Outline each Trypanosoma brucei.
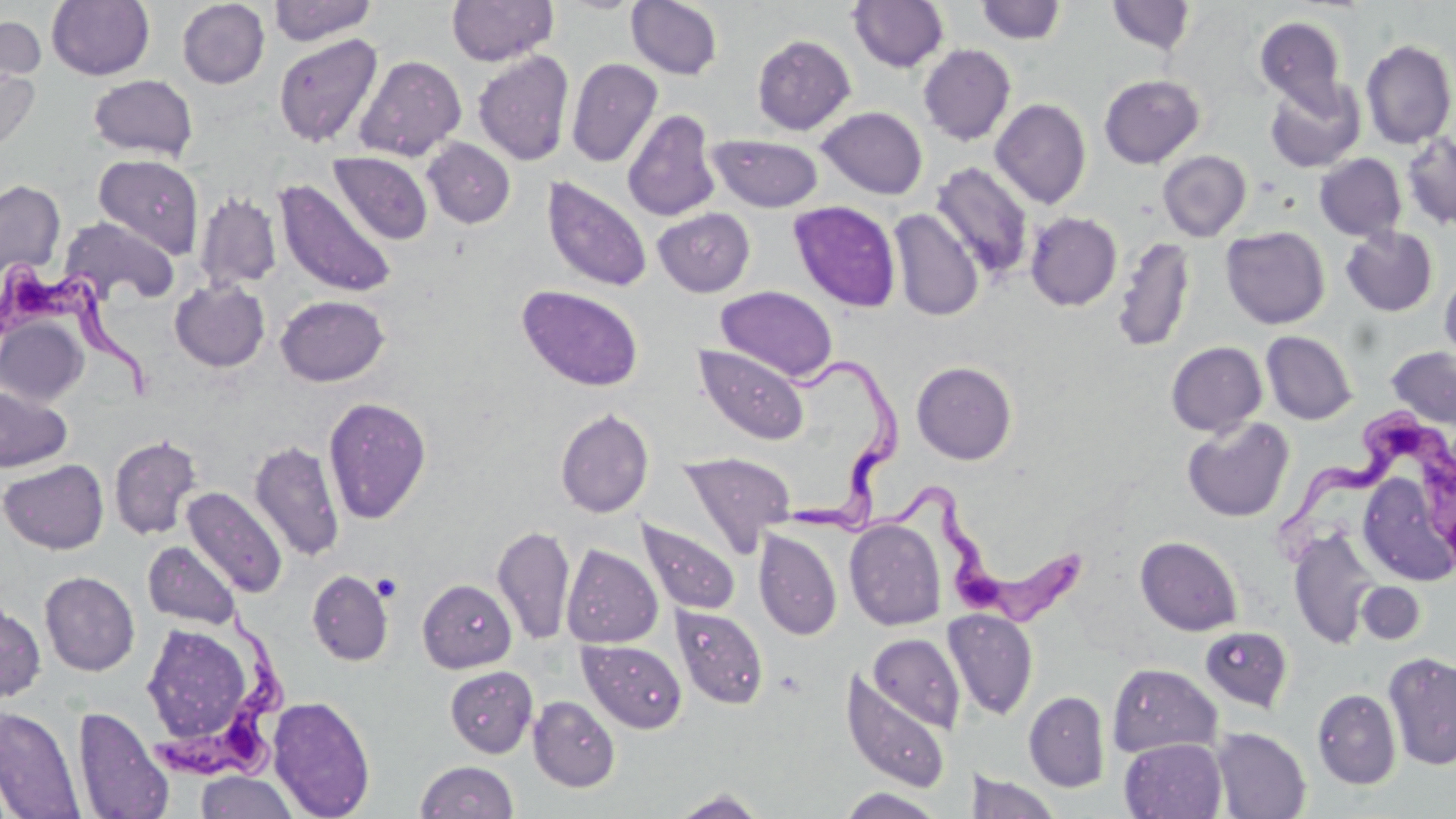
Approximate bounding boxes as named x1/y1/x2/y2 corners in pixels.
Trypanosoma brucei: (x1=1, y1=257, x2=162, y2=401), (x1=771, y1=350, x2=910, y2=549), (x1=1279, y1=411, x2=1453, y2=558), (x1=878, y1=484, x2=1083, y2=635), (x1=151, y1=608, x2=290, y2=785).

{
  "slide_level_diagnosis": "Trypanosoma brucei",
  "field_of_view": "one of a larger specimen",
  "modality": "light microscopy",
  "image_size": "1456×819 pixels",
  "magnification": "1000x",
  "uninfected_red_blood_cell_locations": "approximate bounding boxes as named x1/y1/x2/y2 corners in pixels: (x1=47, y1=0, x2=154, y2=80), (x1=269, y1=0, x2=377, y2=45), (x1=447, y1=0, x2=559, y2=66), (x1=627, y1=0, x2=723, y2=79), (x1=848, y1=0, x2=949, y2=73), (x1=177, y1=1, x2=269, y2=88), (x1=976, y1=1, x2=1067, y2=44), (x1=1106, y1=1, x2=1197, y2=55), (x1=0, y1=14, x2=46, y2=94), (x1=1255, y1=16, x2=1348, y2=115), (x1=273, y1=33, x2=383, y2=147), (x1=751, y1=34, x2=856, y2=134), (x1=1361, y1=39, x2=1455, y2=149), (x1=918, y1=44, x2=1016, y2=145), (x1=472, y1=49, x2=574, y2=166), (x1=354, y1=55, x2=467, y2=162), (x1=566, y1=57, x2=662, y2=168), (x1=0, y1=61, x2=40, y2=159), (x1=88, y1=74, x2=198, y2=160), (x1=1098, y1=74, x2=1205, y2=168), (x1=1264, y1=77, x2=1363, y2=172), (x1=991, y1=98, x2=1091, y2=209), (x1=817, y1=106, x2=928, y2=199), (x1=622, y1=109, x2=721, y2=222), (x1=1401, y1=133, x2=1456, y2=230), (x1=707, y1=134, x2=824, y2=212), (x1=422, y1=138, x2=515, y2=228), (x1=1158, y1=150, x2=1251, y2=241), (x1=329, y1=152, x2=434, y2=244), (x1=92, y1=153, x2=204, y2=258), (x1=1315, y1=153, x2=1406, y2=241), (x1=930, y1=162, x2=1035, y2=281), (x1=542, y1=176, x2=653, y2=293), (x1=0, y1=179, x2=66, y2=282), (x1=275, y1=179, x2=397, y2=298), (x1=195, y1=191, x2=281, y2=291), (x1=788, y1=200, x2=902, y2=313), (x1=652, y1=207, x2=755, y2=297), (x1=889, y1=208, x2=984, y2=321), (x1=1025, y1=212, x2=1122, y2=311), (x1=58, y1=216, x2=179, y2=306), (x1=1221, y1=226, x2=1330, y2=329), (x1=1340, y1=226, x2=1438, y2=317), (x1=1112, y1=236, x2=1196, y2=354), (x1=1439, y1=268, x2=1456, y2=367), (x1=170, y1=279, x2=270, y2=372), (x1=517, y1=284, x2=643, y2=392), (x1=716, y1=286, x2=838, y2=383), (x1=275, y1=295, x2=389, y2=386), (x1=0, y1=318, x2=88, y2=406), (x1=1261, y1=331, x2=1357, y2=425), (x1=1166, y1=342, x2=1267, y2=437), (x1=694, y1=344, x2=809, y2=445), (x1=1386, y1=346, x2=1456, y2=430), (x1=911, y1=361, x2=1017, y2=465), (x1=0, y1=385, x2=72, y2=474), (x1=322, y1=396, x2=432, y2=524), (x1=555, y1=408, x2=655, y2=518), (x1=1182, y1=417, x2=1295, y2=522), (x1=108, y1=434, x2=203, y2=541), (x1=249, y1=440, x2=345, y2=561), (x1=678, y1=451, x2=796, y2=556), (x1=0, y1=459, x2=108, y2=554), (x1=1361, y1=472, x2=1451, y2=589), (x1=183, y1=486, x2=287, y2=598), (x1=844, y1=518, x2=946, y2=631), (x1=639, y1=521, x2=740, y2=615), (x1=492, y1=525, x2=575, y2=645), (x1=753, y1=528, x2=842, y2=640), (x1=1289, y1=529, x2=1380, y2=648), (x1=1135, y1=536, x2=1242, y2=636), (x1=143, y1=541, x2=241, y2=629), (x1=562, y1=544, x2=663, y2=648), (x1=307, y1=569, x2=394, y2=666), (x1=39, y1=571, x2=140, y2=676), (x1=418, y1=579, x2=517, y2=673), (x1=1357, y1=582, x2=1425, y2=644), (x1=0, y1=599, x2=46, y2=703), (x1=672, y1=605, x2=768, y2=710), (x1=943, y1=608, x2=1039, y2=720), (x1=137, y1=618, x2=250, y2=738), (x1=1200, y1=627, x2=1294, y2=713), (x1=868, y1=633, x2=965, y2=732), (x1=578, y1=639, x2=687, y2=733), (x1=1382, y1=651, x2=1456, y2=771), (x1=1107, y1=663, x2=1222, y2=758), (x1=445, y1=666, x2=538, y2=757), (x1=840, y1=668, x2=953, y2=794), (x1=1312, y1=688, x2=1402, y2=789), (x1=1024, y1=690, x2=1110, y2=791), (x1=267, y1=695, x2=376, y2=818), (x1=528, y1=696, x2=620, y2=792), (x1=73, y1=705, x2=174, y2=819), (x1=0, y1=706, x2=86, y2=819), (x1=1211, y1=727, x2=1310, y2=818), (x1=1119, y1=737, x2=1227, y2=819), (x1=415, y1=760, x2=519, y2=818), (x1=967, y1=770, x2=1061, y2=819), (x1=194, y1=771, x2=299, y2=818), (x1=837, y1=787, x2=946, y2=818), (x1=669, y1=789, x2=769, y2=818)",
  "stain": "May-Grünwald-Giemsa",
  "preparation": "thin blood smear"
}